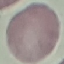
Malaria status: uninfected. Automatically extracted cell patch, resized to 64 × 64 pixels. Giemsa-stained preparation. Thin blood smear. Acquired by smartphone through the microscope eyepiece.